Assess the morphology of the erythrocytes.
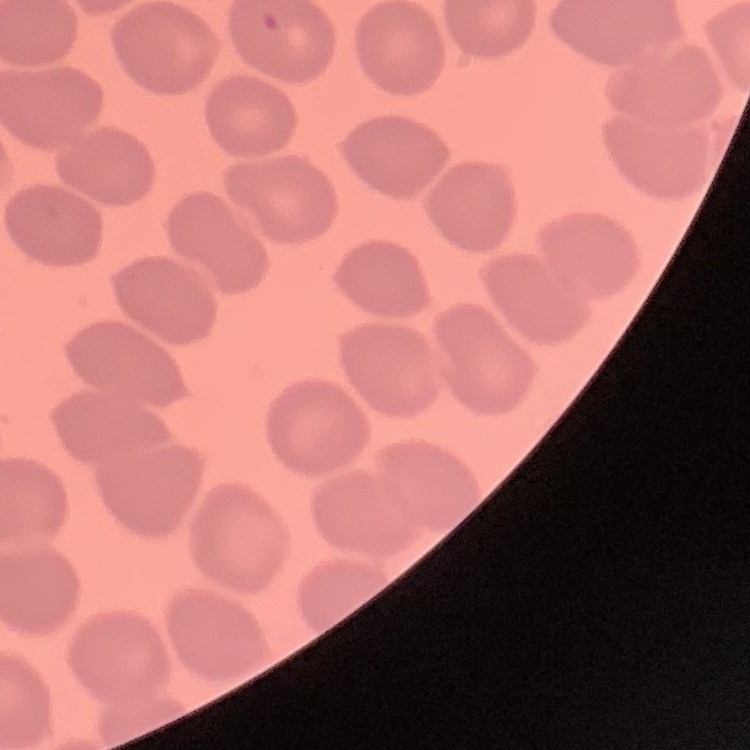

No rouleaux formation.

Summary:
  - Stain: Field's or Giemsa
  - Image type: square crop of a larger photomicrograph
  - Preparation: thin blood smear